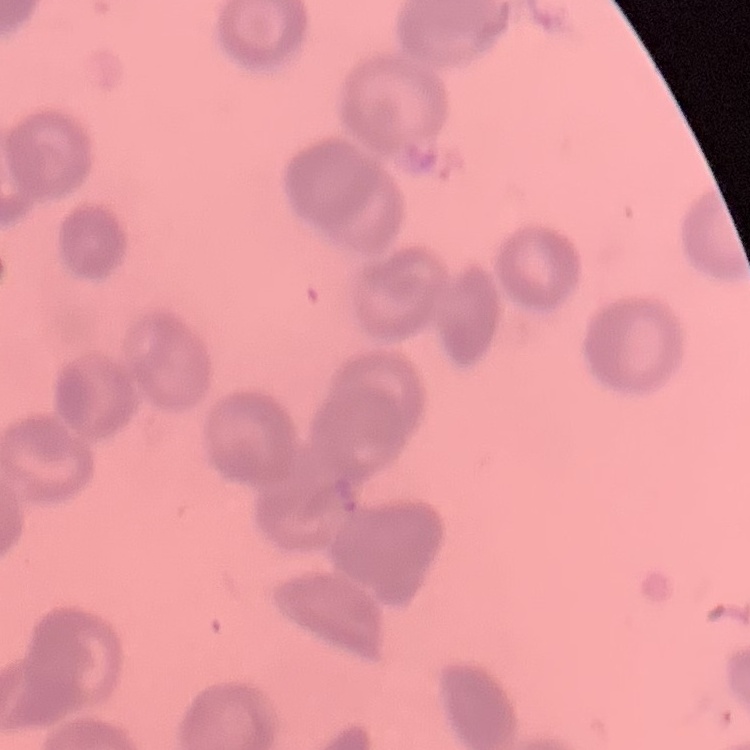
Summary:
  - Red blood cell morphology: rouleaux formation
  - Stain: Field's or Giemsa
  - Preparation: thin blood film
  - Image type: one tile cut from a larger photomicrograph